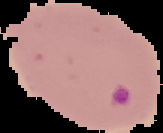
From a thin blood smear. Result: Plasmodium parasites detected. Segmented cell region on a black background. Image is 163×133 pixels.